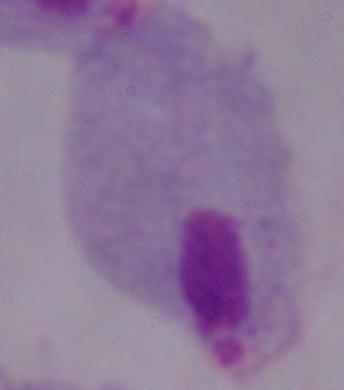
Summary:
  - Modality: micrograph
  - Magnification: 1000x
  - Identification: trichomonad